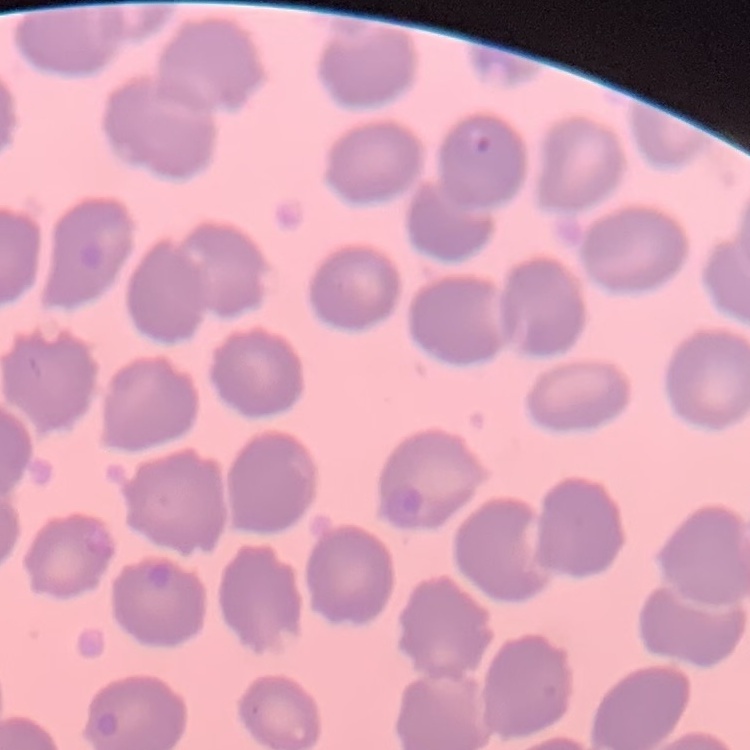 The red blood cells exhibit no rouleaux formation. Stained with either Field's or Giemsa. One tile cut from a larger photomicrograph. Thin blood smear.